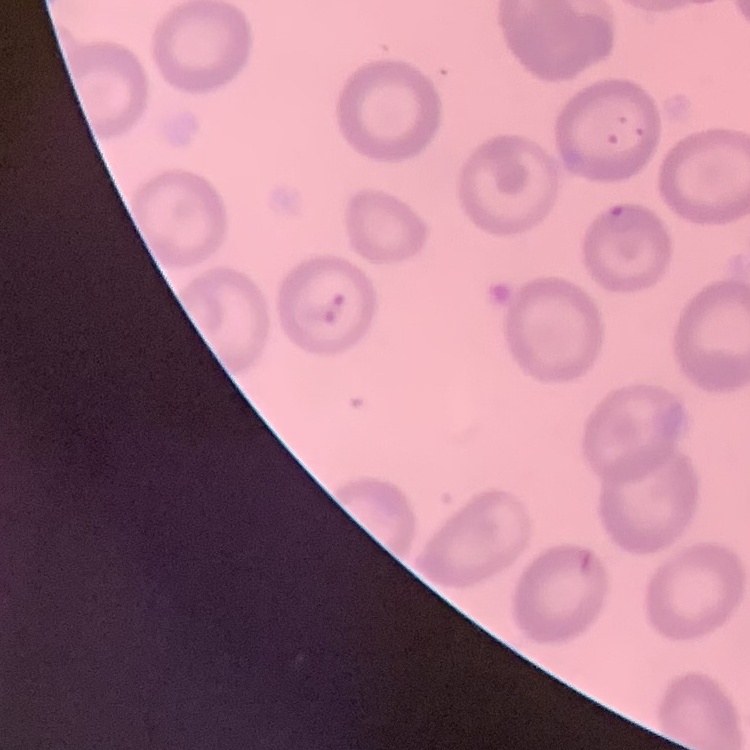
Summary:
  - Erythrocyte morphology: no rouleaux formation
  - Preparation: thin blood film
  - Stain: Field's or Giemsa
  - Image type: square crop of a larger photomicrograph